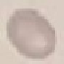
Malaria status: uninfected. Automatically extracted cell patch, resized to 64 × 64 pixels. Giemsa-stained preparation. Thin blood smear. Photographed with a smartphone camera at the microscope eyepiece.